Outline every Plasmodium parasite.
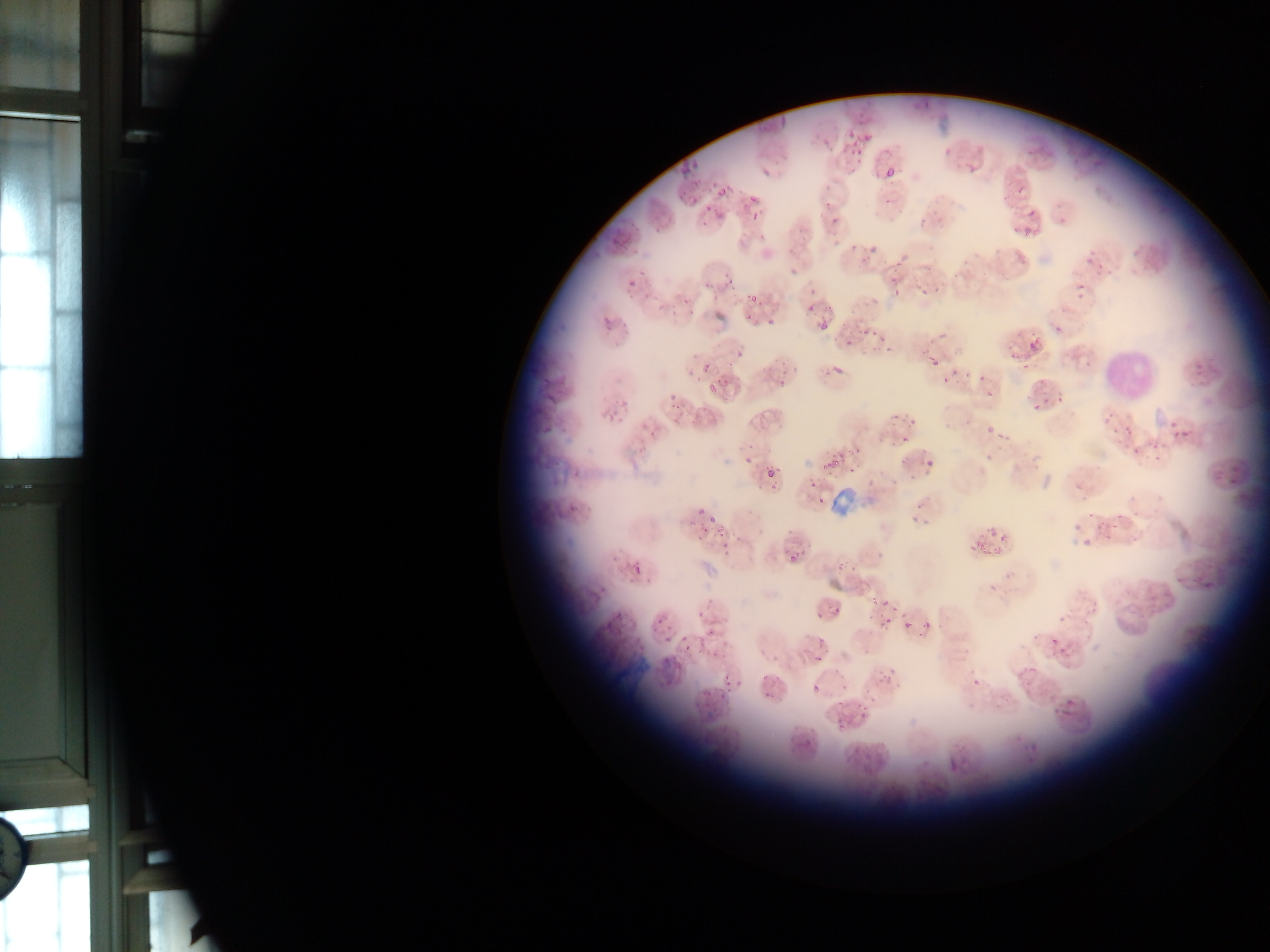

Approximate bounding boxes as {left, top, right, bottom} in pixels.
Plasmodium parasites (some below the resolvable threshold): {846, 123, 861, 151}, {881, 154, 896, 179}, {673, 161, 699, 195}, {713, 172, 737, 202}, {744, 192, 775, 239}, {701, 198, 724, 218}, {624, 262, 645, 295}, {712, 277, 733, 291}, {915, 282, 933, 298}, {662, 293, 686, 313}, {742, 293, 757, 304}, {595, 303, 614, 329}, {749, 312, 764, 323}, {807, 319, 829, 330}, {853, 322, 875, 335}, {732, 346, 751, 361}, {826, 346, 848, 381}, {924, 353, 938, 366}, {701, 360, 713, 372}, {762, 363, 784, 394}, {931, 375, 965, 401}, {705, 380, 730, 400}, {979, 382, 993, 405}, {667, 394, 681, 408}, {602, 398, 631, 419}, {688, 404, 705, 418}, {906, 408, 920, 438}, {977, 424, 993, 448}, {1173, 426, 1192, 443}, {895, 435, 910, 446}, {741, 439, 756, 467}, {820, 449, 847, 475}, {922, 454, 951, 477}, {763, 464, 780, 483}, {570, 483, 591, 504}, {815, 493, 830, 509}, {911, 511, 931, 538}, {705, 515, 719, 525}, {979, 520, 1004, 570}, {1066, 522, 1092, 537}, {721, 529, 739, 548}, {1070, 541, 1097, 571}, {626, 551, 650, 572}, {782, 551, 799, 569}, {965, 552, 970, 560}, {818, 594, 832, 611}, {877, 595, 894, 613}, {901, 600, 923, 639}, {659, 609, 673, 632}, {911, 611, 936, 643}, {874, 613, 892, 626}, {709, 622, 732, 653}, {1046, 628, 1065, 654}, {675, 631, 693, 656}, {805, 636, 827, 661}, {649, 645, 673, 679}, {836, 659, 858, 694}, {805, 676, 829, 690}, {1062, 694, 1086, 724}, {854, 702, 874, 724}, {1023, 746, 1040, 766}, {944, 753, 968, 777}.

{
  "leukocyte_locations": "approximate bounding boxes as {left, top, right, bottom} in pixels: {1097, 336, 1162, 409}",
  "country": "Ghana",
  "field_of_view": "single",
  "capture": "mobile-phone photograph through a microscope",
  "image_size": "1270×952 pixels",
  "preparation": "thin blood film"
}